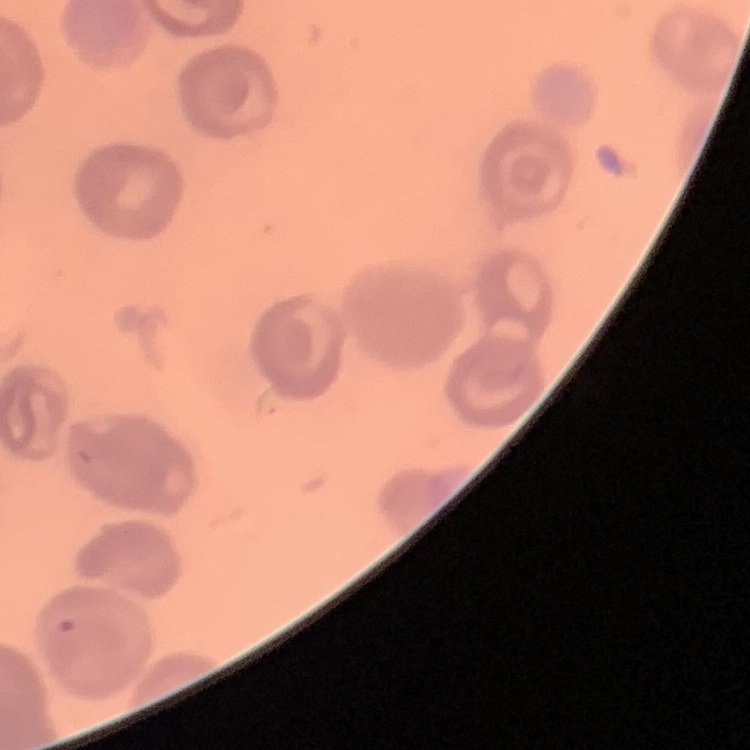
The red blood cells show no rouleaux formation. Stained with either Field's or Giemsa. Thin blood smear. Square crop of a larger photomicrograph.